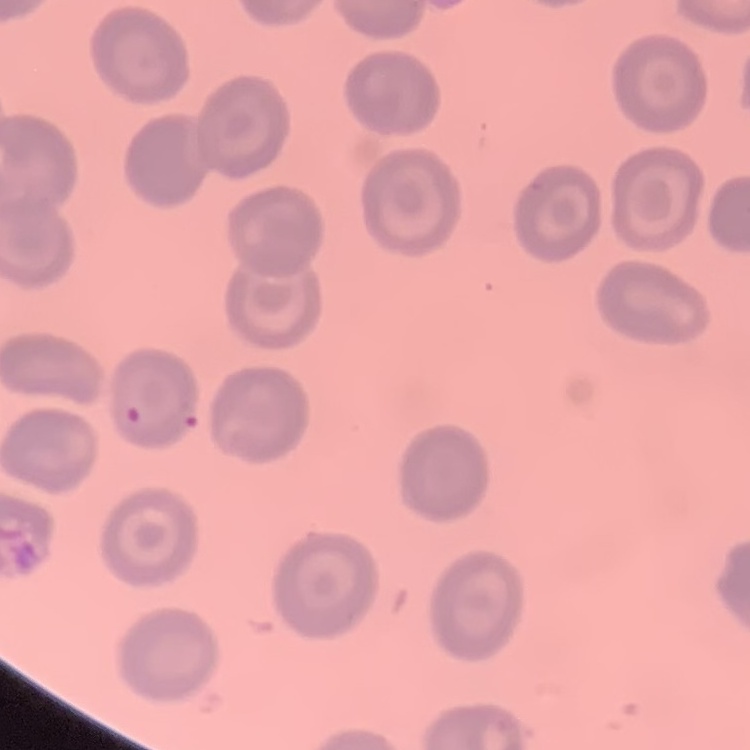
The erythrocytes exhibit no rouleaux formation. Stained with either Field's or Giemsa. One tile cut from a larger photomicrograph. Thin blood film.